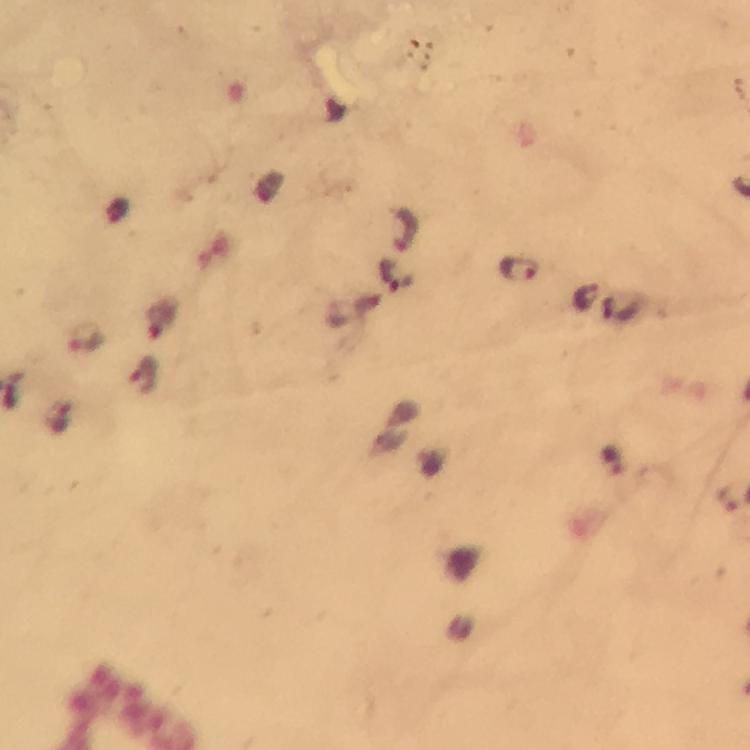

{
  "immersion_oil": "used",
  "cropped_from": "a single field of view",
  "malaria_parasite_locations": "approximate centers as [x, y] in pixels: [405, 231], [517, 268], [398, 278], [159, 320], [86, 339], [145, 375]",
  "preparation": "thick blood smear",
  "capture": "smartphone camera through the microscope",
  "magnification": "100x",
  "image_size": "750×750 pixels",
  "stain": "Giemsa",
  "context": "from a malaria diagnostic workup"
}